Name the cell type shown.
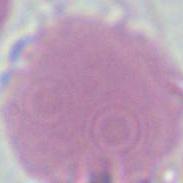
An erythrocyte.

Summary:
  - Magnification: 1000x
  - Modality: photomicrograph